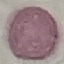

result = no malaria parasites seen
stain = Giemsa
image type = automatically extracted cell patch, resized to 64 × 64 pixels
preparation = thin smear
capture = smartphone through the microscope eyepiece